Identify the parasite.
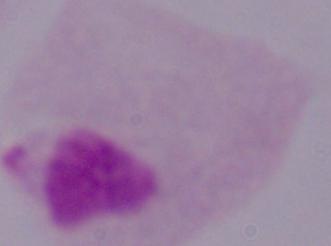

This is a trichomonad.

Micrograph. Captured at 1000x magnification.